Assess for parasitized red blood cells.
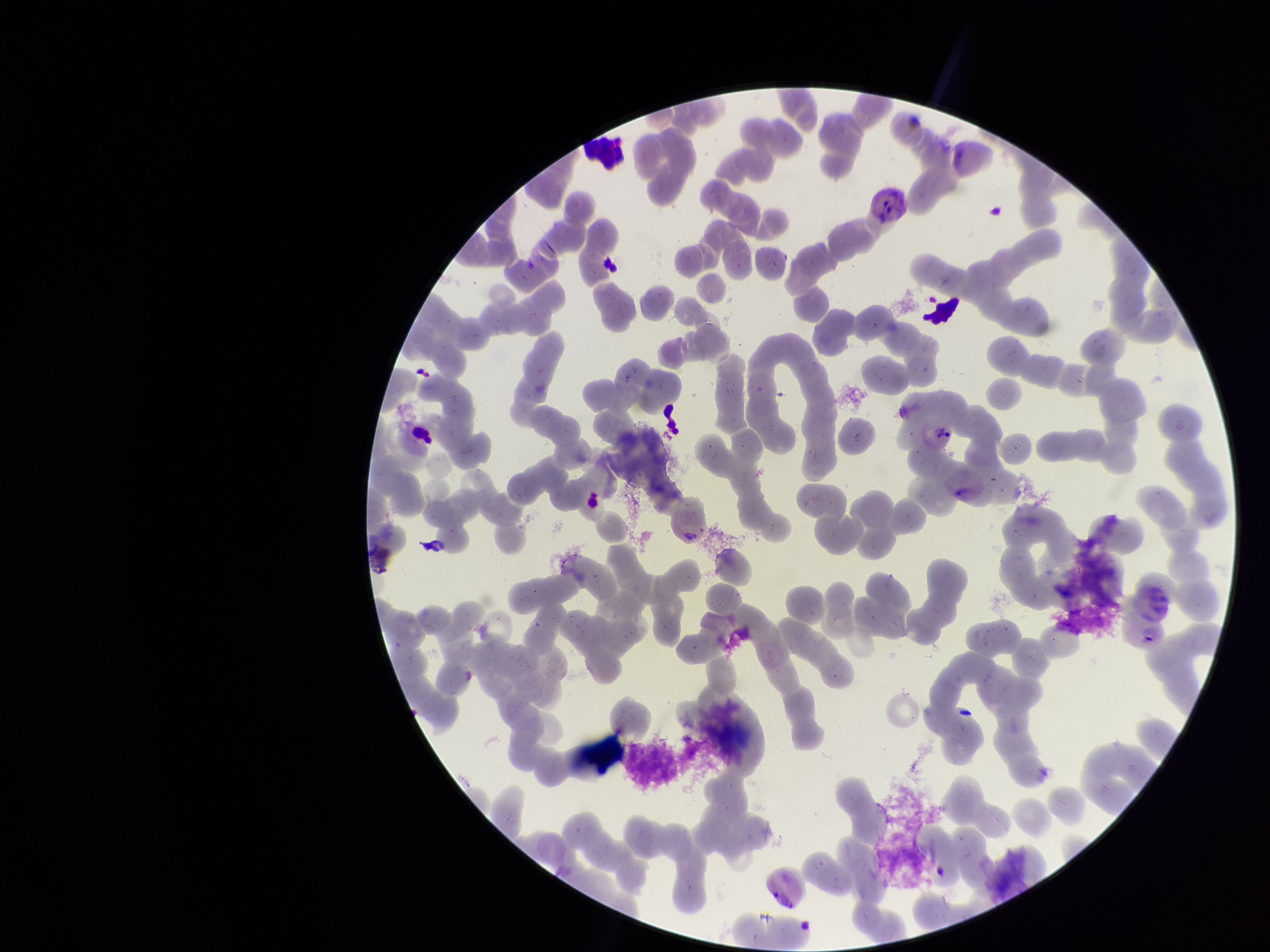

None detected.

Parasitized red blood cell count: 0. Species reported for this patient: Plasmodium vivax. Image is 1270×952 pixels. Smartphone photograph taken through the eyepiece of a microscope. Preparation: thin. Single field of view. Red blood cell count: 218. Giemsa stain. Patient malaria status: positive.